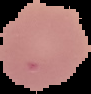

From a thin blood smear. Cell region segmented out of the field of view; the surrounding area is masked to black. Image is 91×94 pixels. Malaria status: uninfected.